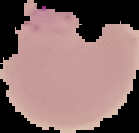

Summary:
  - Image size: 139×133 pixels
  - Preparation: thin blood film
  - Malaria status: parasitized
  - Image type: cell region segmented out of the field of view; surrounding area masked to black